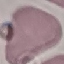
malaria status = uninfected
preparation = thin blood smear
stain = Giemsa
image type = automatically extracted cell patch, resized to 64 × 64 pixels
capture = smartphone through the microscope eyepiece